State which parasite is depicted.
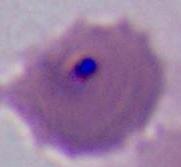

This is Plasmodium.

400x or 1000x magnification. Photomicrograph.